Locate every Plasmodium parasite.
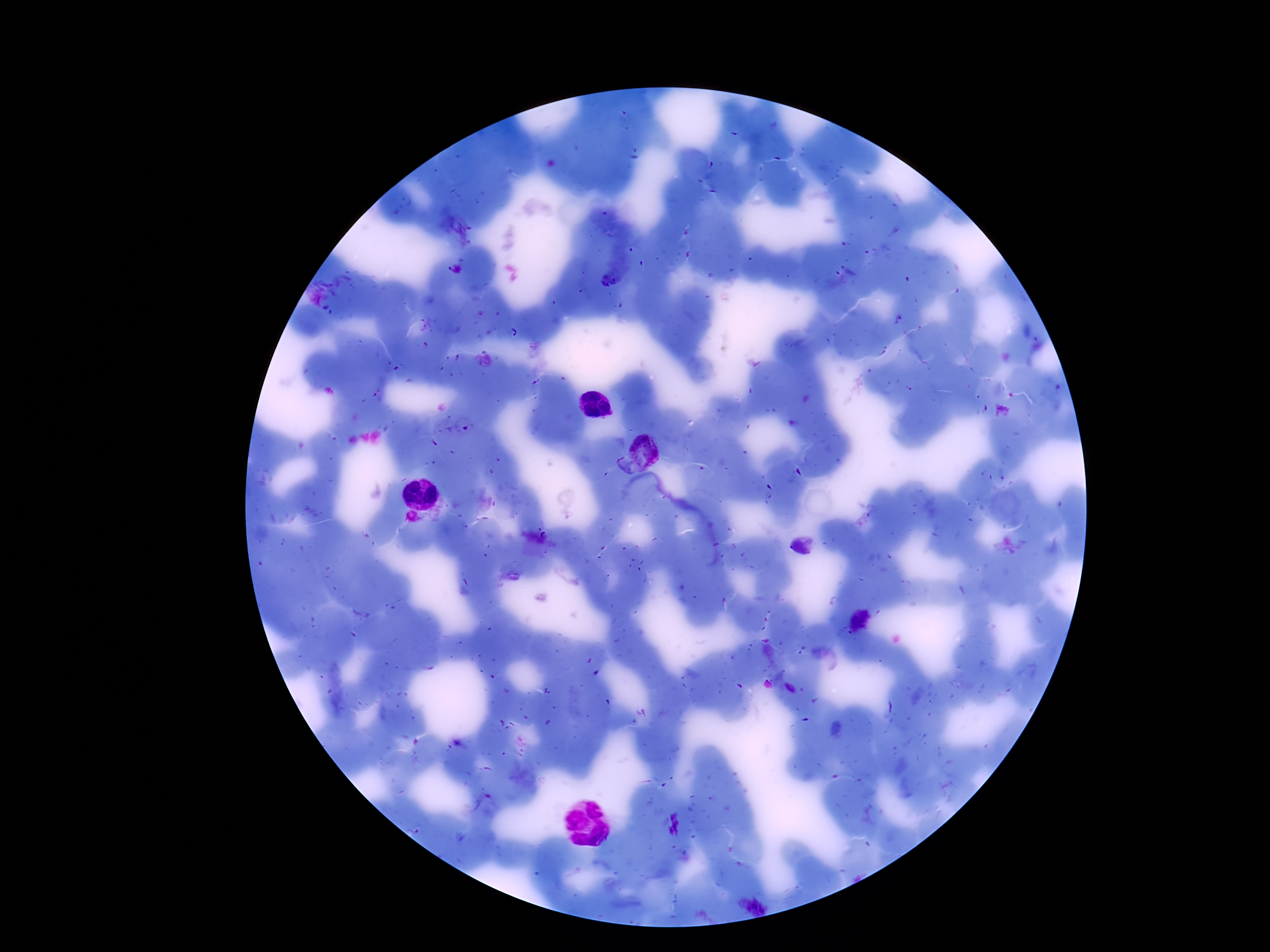
Approximate centers as (x, y) in pixels.
Plasmodium parasites: (454, 269), (646, 450), (625, 469).

Image is 1270×952 pixels. One field from this slide. Giemsa-stained preparation. 100x magnification. Patient malaria status: infected. Smartphone photograph taken through the microscope eyepiece. Thick peripheral-blood smear.